Comment on the morphology of the erythrocytes.
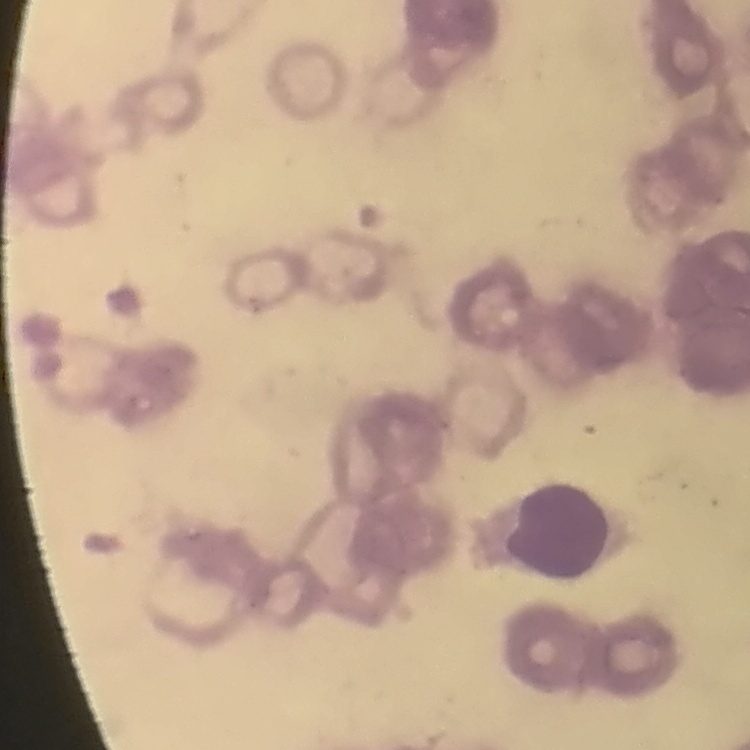
Rouleaux formation.

{
  "preparation": "thin peripheral smear",
  "image_type": "one tile cut from a larger photomicrograph",
  "stain": "Field's or Giemsa"
}